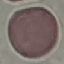

{
  "result": "no malaria parasites seen",
  "stain": "Giemsa",
  "capture": "smartphone through the microscope eyepiece",
  "image_type": "cell patch, automatically extracted from a larger field of view and resized to 64 × 64 pixels",
  "preparation": "thin smear"
}